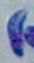

Summary:
  - Identification: Toxoplasma gondii
  - Magnification: 1000x
  - Modality: photomicrograph